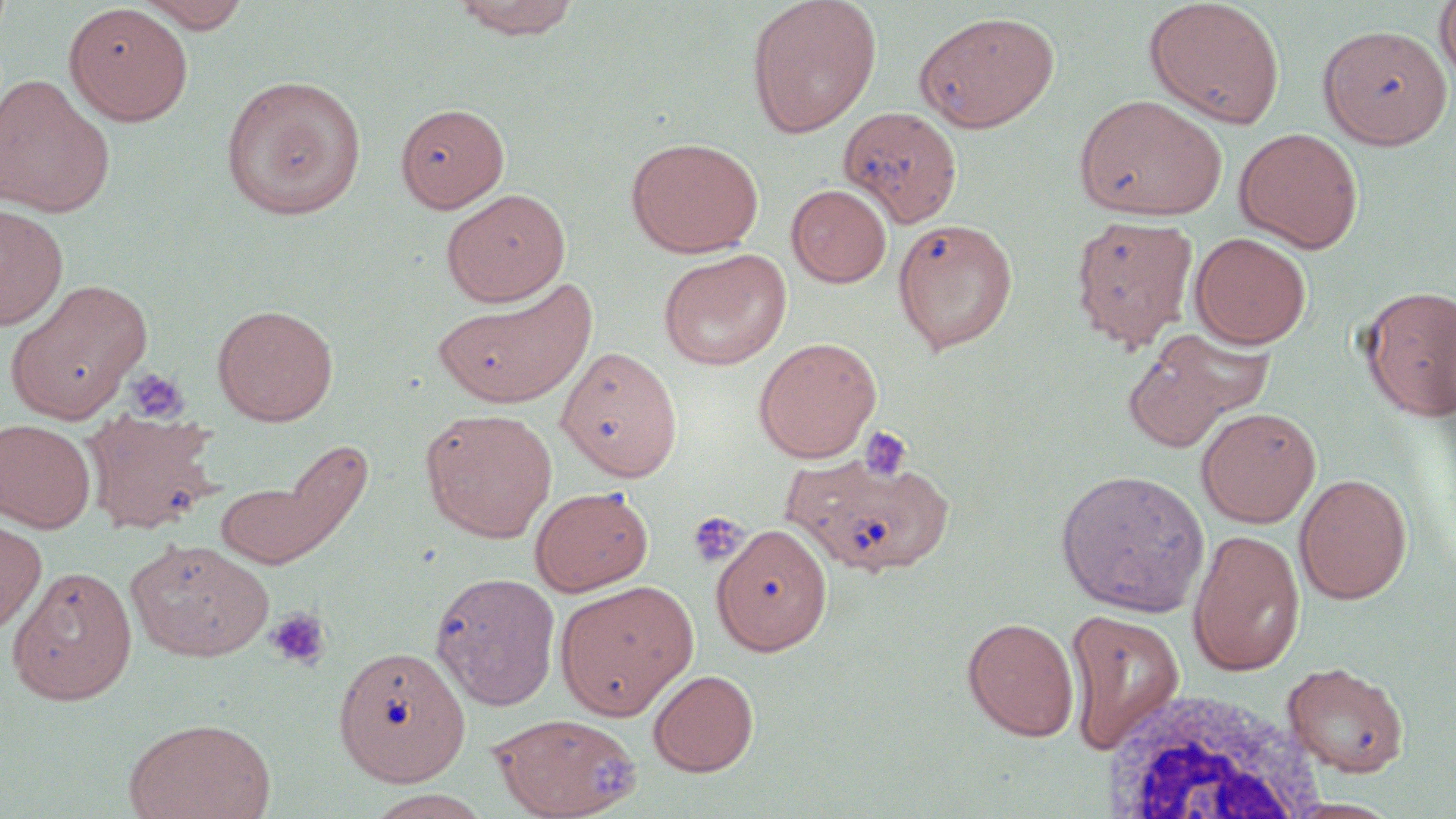 Approximate bounding boxes as [x1, y1, x2, y2] in pixels. Platelet locations: [124, 367, 189, 424], [857, 425, 912, 483], [688, 511, 749, 567], [265, 606, 331, 671], [586, 742, 643, 803]. White blood cell locations: [1105, 687, 1327, 819]. Uninfected red blood cell locations: [136, 0, 253, 32], [449, 0, 585, 40], [746, 0, 882, 137], [1144, 0, 1286, 129], [1434, 1, 1456, 87], [63, 3, 194, 125], [914, 10, 1060, 133], [1318, 24, 1453, 150], [0, 73, 115, 217], [221, 74, 366, 219], [1073, 94, 1228, 221], [395, 100, 511, 217], [839, 105, 963, 228], [1234, 127, 1363, 253], [625, 136, 764, 257], [786, 184, 892, 287], [441, 188, 570, 306], [0, 203, 68, 331], [1069, 214, 1200, 351], [893, 217, 1019, 355], [1190, 232, 1311, 348], [656, 249, 792, 371], [432, 278, 596, 409], [3, 280, 152, 425], [1358, 284, 1455, 422], [211, 303, 338, 426], [753, 336, 882, 463], [1123, 336, 1245, 453], [556, 345, 684, 482], [1196, 406, 1321, 527], [81, 407, 222, 535], [421, 408, 558, 542], [0, 418, 96, 532], [216, 440, 370, 571], [784, 450, 956, 577], [1055, 468, 1209, 617], [1294, 472, 1413, 604], [529, 485, 654, 596], [0, 516, 46, 638], [712, 521, 833, 657], [1187, 529, 1305, 677], [126, 538, 274, 662], [6, 564, 138, 705], [430, 571, 561, 710], [554, 578, 699, 719], [1064, 609, 1185, 753], [962, 616, 1079, 741], [333, 644, 471, 786], [1283, 662, 1410, 776], [648, 669, 759, 776], [490, 712, 642, 819], [123, 716, 276, 819], [362, 790, 495, 818]. Slide-level diagnosis: negative for blood parasites. Single field of view. Optical microscopy. May-Grünwald-Giemsa stain. Image is 1456×819 pixels. Thin blood smear. 1000x magnification.